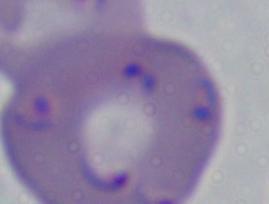
A Babesia parasite is shown. Photomicrograph. 1000x magnification.